State which parasite is depicted.
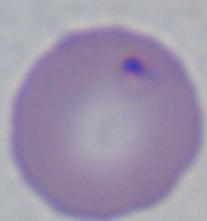

This is Babesia.

Summary:
  - Modality: micrograph
  - Magnification: 1000x